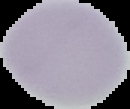 From a thin blood film. Segmented cell region on a black background. Image is 130×109 pixels. Result: no Plasmodium parasites seen.